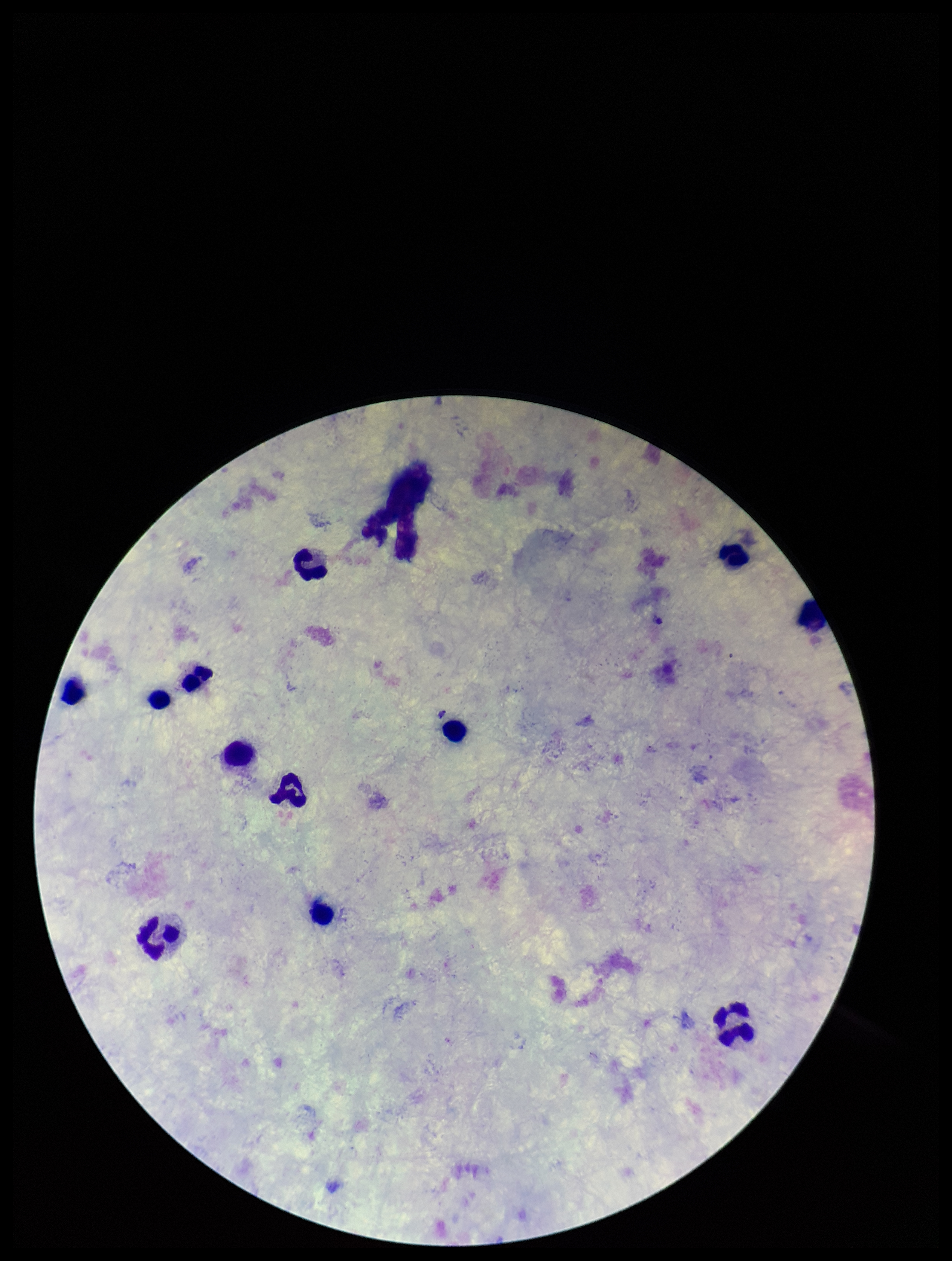

image size = 952×1261 pixels
parasite count = 0
stain = Giemsa
capture = smartphone photograph through the microscope eyepiece
patient malaria status = negative
field of view = one from this slide
preparation = thick blood smear
leukocyte count = 12
Plasmodium parasites = none seen